Locate and identify every blood parasite.
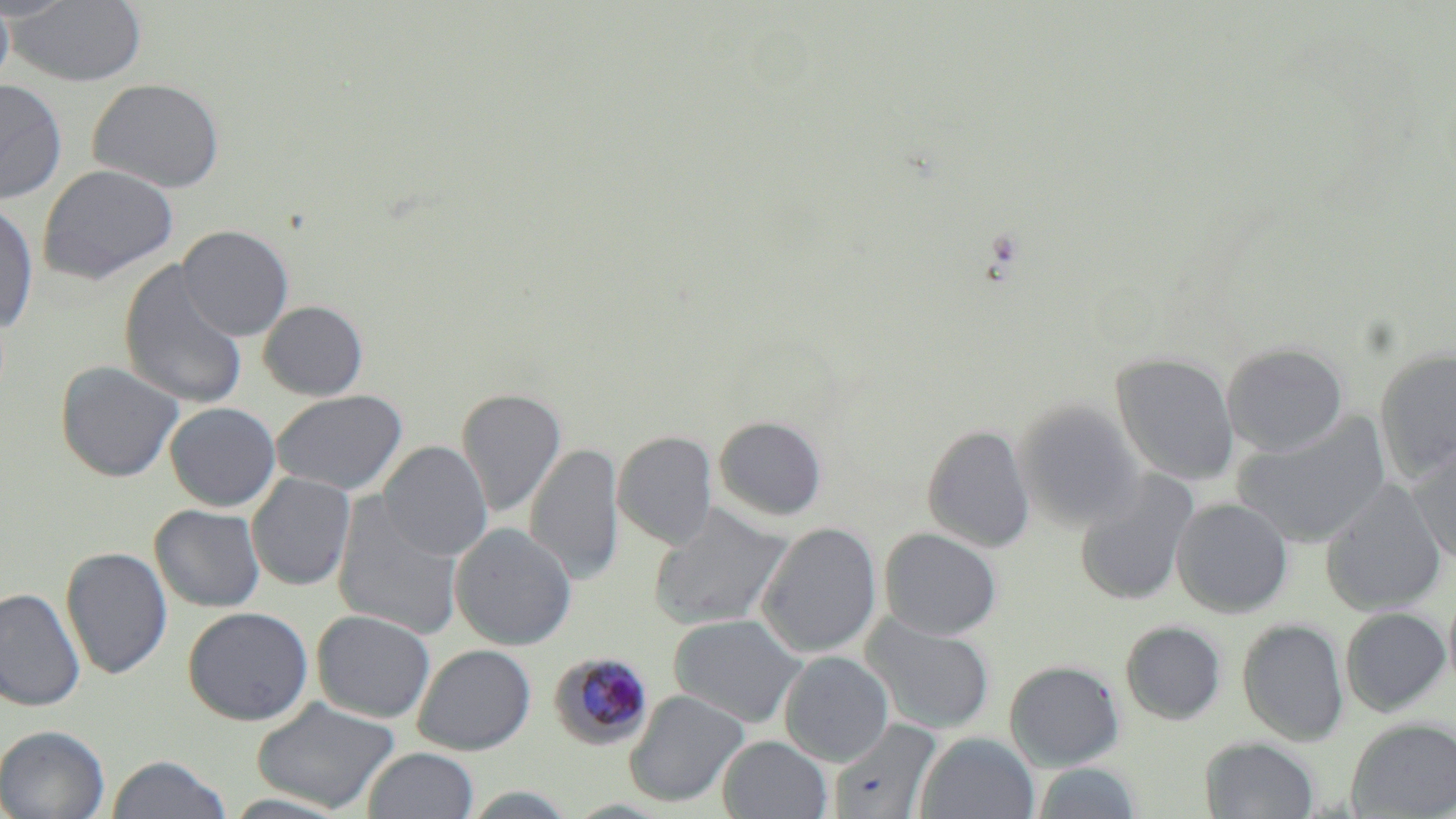

Approximate bounding boxes as (x1, y1, x2, y2) in pixels.
Plasmodium malariae-infected red blood cells: (550, 652, 654, 749).
No Plasmodium falciparum, Plasmodium ovale, Plasmodium vivax, Babesia divergens, or Trypanosoma brucei observed.

Summary:
  - Uninfected red blood cell locations: (0, 0, 15, 93), (7, 0, 147, 87), (88, 77, 225, 193), (0, 78, 68, 204), (38, 164, 179, 284), (0, 200, 39, 334), (176, 224, 294, 341), (118, 259, 248, 410), (259, 300, 368, 400), (1222, 342, 1349, 458), (1374, 347, 1456, 481), (1111, 352, 1239, 485), (55, 360, 183, 482), (457, 388, 566, 517), (271, 389, 408, 495), (1014, 398, 1143, 531), (165, 402, 281, 511), (1233, 412, 1393, 549), (714, 415, 827, 521), (922, 424, 1035, 552), (613, 430, 717, 549), (378, 441, 492, 560), (526, 443, 624, 585), (1407, 445, 1456, 567), (1074, 471, 1198, 606), (247, 472, 356, 591), (1320, 480, 1447, 616), (332, 494, 464, 640), (1171, 497, 1294, 618), (150, 504, 265, 612), (649, 504, 791, 630), (757, 522, 882, 658), (449, 523, 576, 650), (879, 527, 1002, 640), (60, 546, 173, 679), (0, 587, 85, 712), (1444, 590, 1456, 699), (183, 606, 313, 725), (1340, 606, 1451, 716), (312, 609, 435, 722), (669, 614, 806, 728), (862, 614, 996, 735), (1237, 618, 1349, 746), (1120, 620, 1226, 724), (413, 644, 536, 755), (779, 651, 894, 766), (1004, 660, 1125, 770), (624, 690, 748, 808), (251, 697, 400, 813), (1346, 717, 1456, 817), (828, 718, 941, 819), (0, 725, 110, 819), (915, 732, 1039, 819), (717, 735, 831, 818), (1200, 736, 1320, 818), (363, 747, 478, 819), (106, 754, 233, 818), (1033, 761, 1142, 819)
  - Slide-level diagnosis: Plasmodium malariae
  - Image size: 1456×819 pixels
  - Stain: May-Grünwald-Giemsa
  - Magnification: 1000x
  - Field of view: one of a larger specimen
  - Modality: light microscopy
  - Preparation: thin blood film